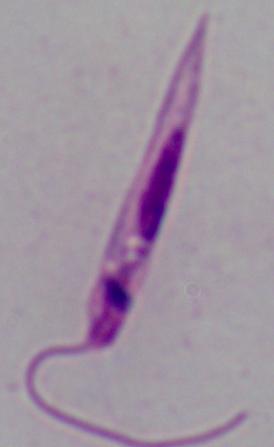

Summary:
  - Magnification: 1000x
  - Identification: Leishmania
  - Modality: micrograph